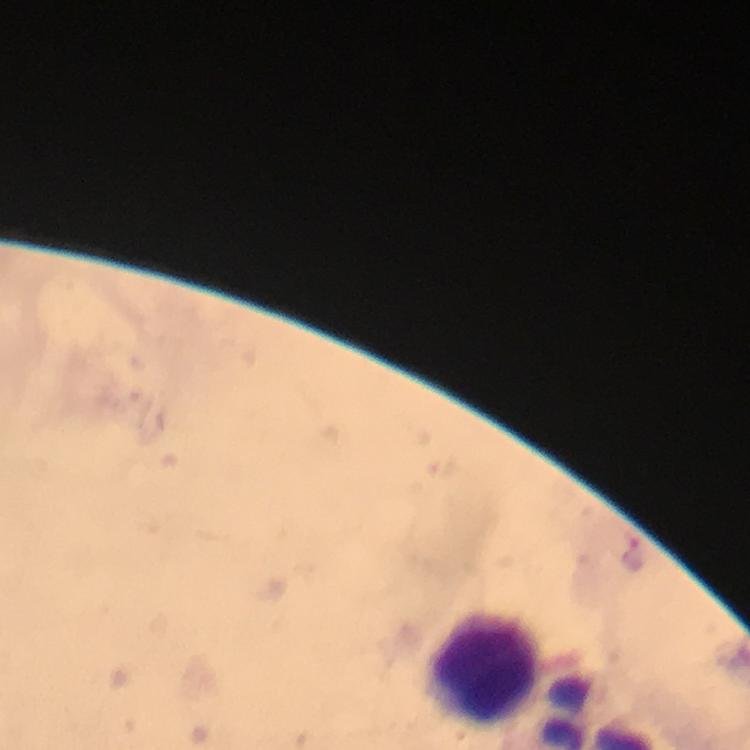

Approximate centers as {x, y} in pixels.
Summary:
  - Leukocyte locations: {484, 665}
  - Plasmodium parasite locations: {636, 555}
  - Cropped from: a single field of view
  - Stain: Giemsa
  - Image size: 750×750 pixels
  - Capture: smartphone photograph through a microscope
  - Preparation: thick blood smear
  - Magnification: 100x
  - Context: from a diagnostic examination for malaria
  - Immersion oil: applied